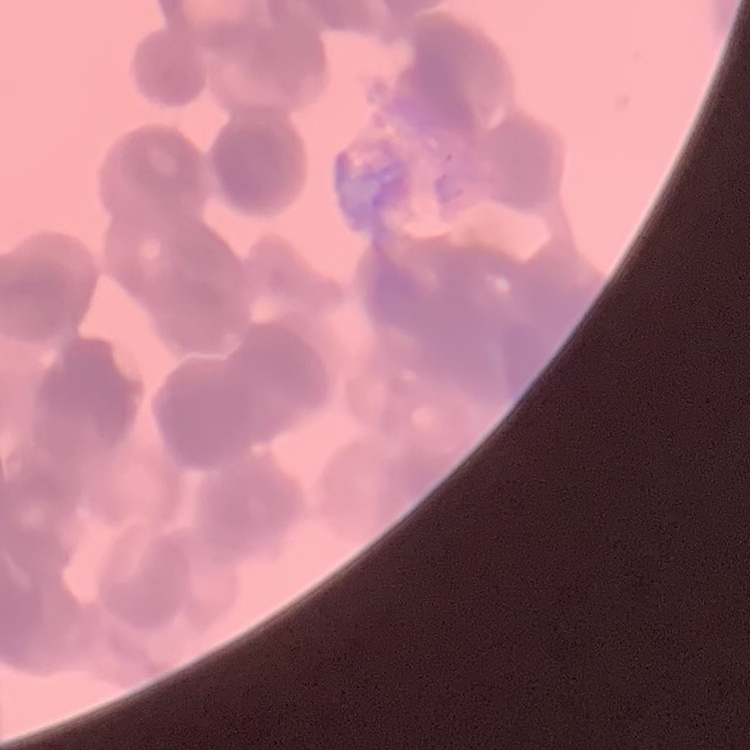

Summary:
  - Erythrocyte morphology: rouleaux formation
  - Preparation: thin blood film
  - Stain: Field's or Giemsa
  - Image type: one tile cut from a larger photomicrograph